Draw a bounding box around every Plasmodium parasite.
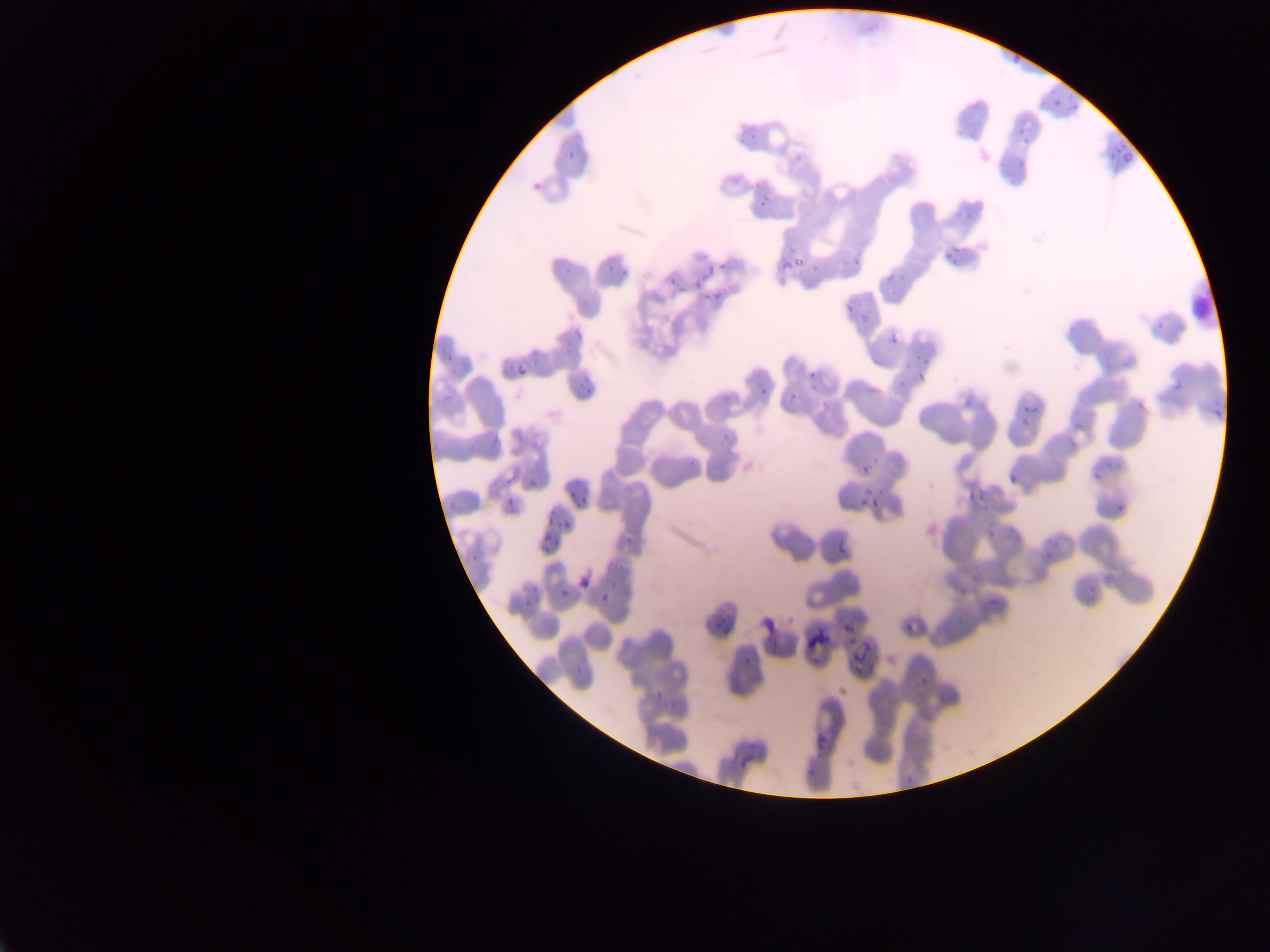
Approximate bounding boxes as left top right bottom in pixels.
Plasmodium parasites: 1063 93 1083 122; 1050 96 1062 110; 1012 117 1035 146; 1106 144 1132 165; 1014 158 1034 175; 730 172 744 193; 528 177 546 196; 753 189 772 213; 852 245 866 268; 942 245 964 259; 781 256 796 267; 793 258 803 269; 598 262 615 275; 720 262 728 270; 704 265 715 273; 808 266 820 279; 881 267 901 288; 614 268 631 279; 664 271 676 288; 694 271 710 286; 680 286 688 292; 710 288 730 310; 836 300 862 319; 558 328 579 342; 887 330 903 347; 441 339 466 364; 919 345 933 368; 514 361 528 379; 571 362 601 397; 914 364 928 382; 807 366 827 384; 754 375 781 402; 896 375 904 389; 1019 385 1045 426; 719 387 738 406; 786 391 801 407; 719 436 731 447; 685 452 700 466; 856 461 878 478; 504 468 521 483; 1005 471 1022 490; 527 476 539 488; 968 484 988 505; 566 488 577 497; 859 488 886 514; 507 496 516 507; 577 496 590 508; 1108 503 1125 518; 546 509 560 524; 561 517 575 532; 1038 520 1069 563; 539 524 559 541; 623 528 639 545; 980 533 1000 545; 542 535 559 554; 575 572 592 592; 527 579 547 595; 558 585 569 601; 952 586 963 598; 595 588 608 600; 519 596 537 607; 759 615 779 635; 836 617 855 634; 899 625 925 642; 738 653 755 669; 902 674 937 698; 651 684 671 699; 818 733 835 753; 738 750 760 768; 805 760 815 781; 898 770 918 789.

Summary:
  - Field of view: single
  - Image size: 1270×952 pixels
  - Country: Ghana
  - Preparation: thin blood film
  - Capture: mobile-phone photograph through a microscope